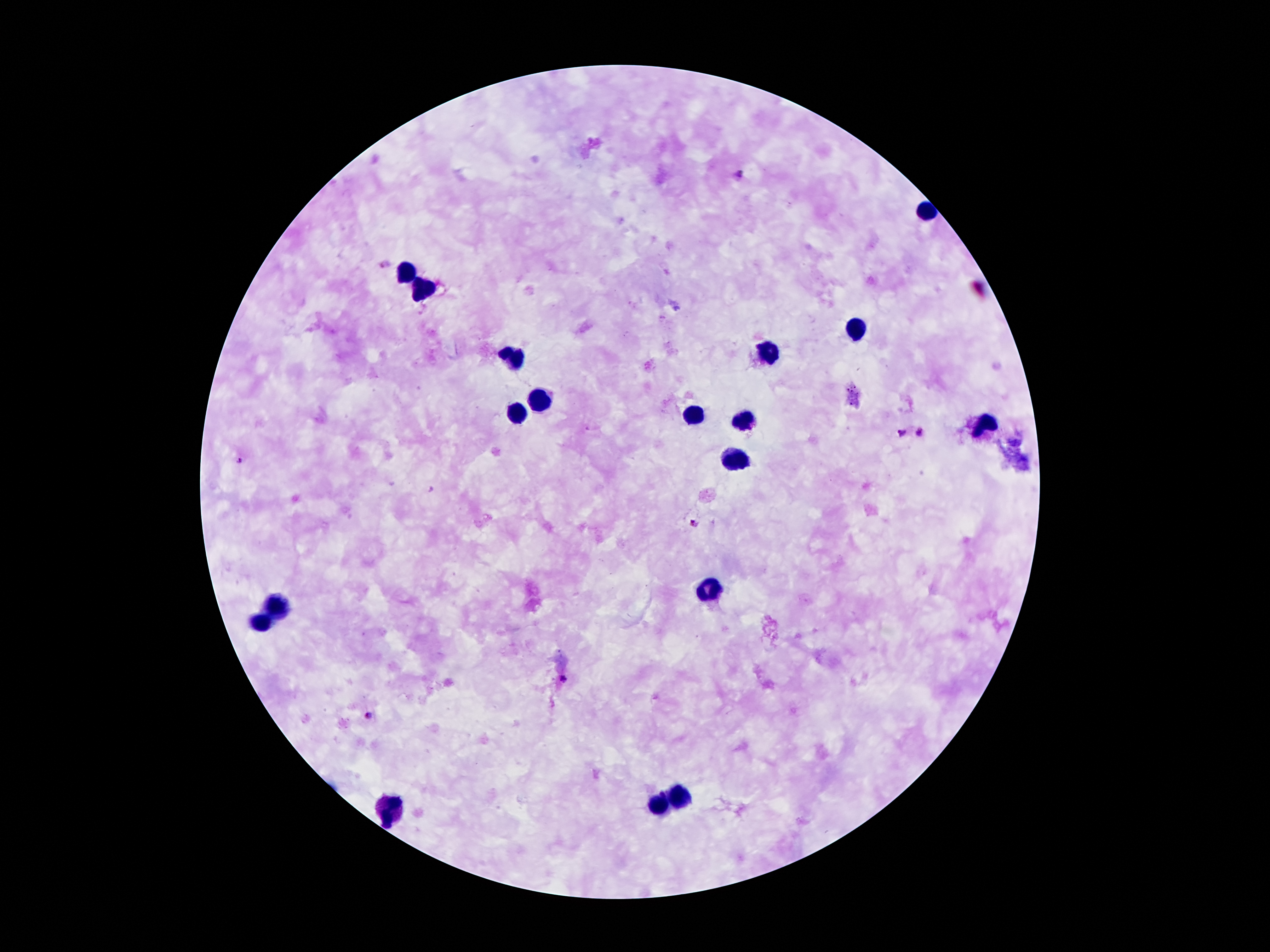
Image is 1270×952 pixels. Smartphone photograph taken through the microscope eyepiece. Giemsa stain. 100x magnification. Patient malaria status: positive for Plasmodium falciparum. Thick blood smear. Single field of view.